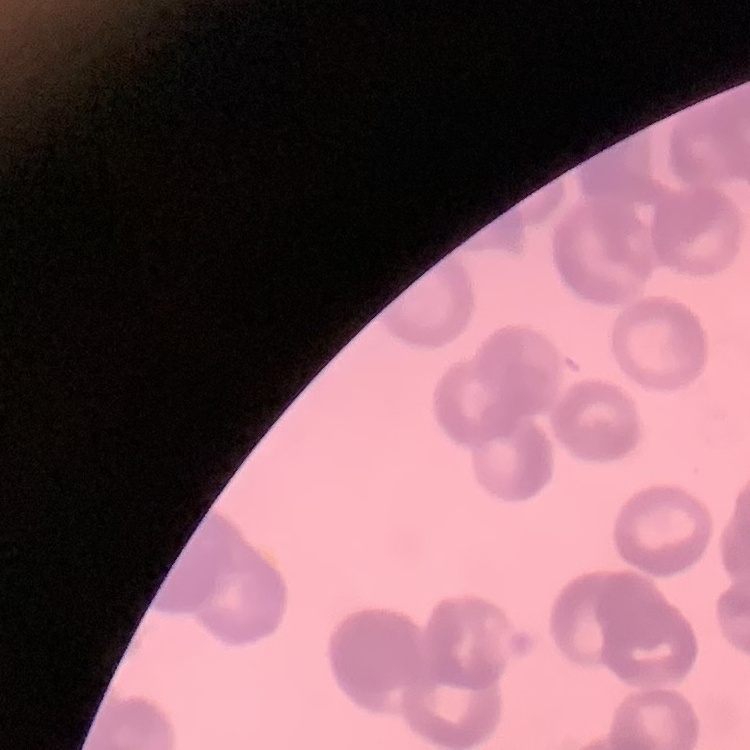

Summary:
  - Red blood cell morphology: rouleaux formation
  - Image type: square crop of a larger photomicrograph
  - Stain: Field's or Giemsa
  - Preparation: thin peripheral smear